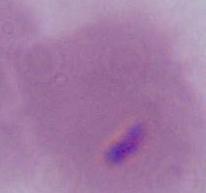 A Plasmodium parasite is seen. 400x or 1000x magnification. Photomicrograph.